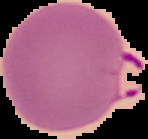

Summary:
  - Image size: 148×139 pixels
  - Image type: segmented cell region on a black background
  - Preparation: thin blood smear
  - Malaria status: parasitized